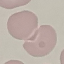

malaria status = uninfected
image type = cell patch, automatically extracted from a larger field of view and resized to 64 × 64 pixels
stain = Giemsa
capture = smartphone through the microscope eyepiece
preparation = thin blood film